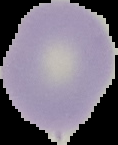 From a thin blood smear. The area outside the segmented cell region is set to black. Image is 118×145 pixels. Result: negative for malaria parasites.